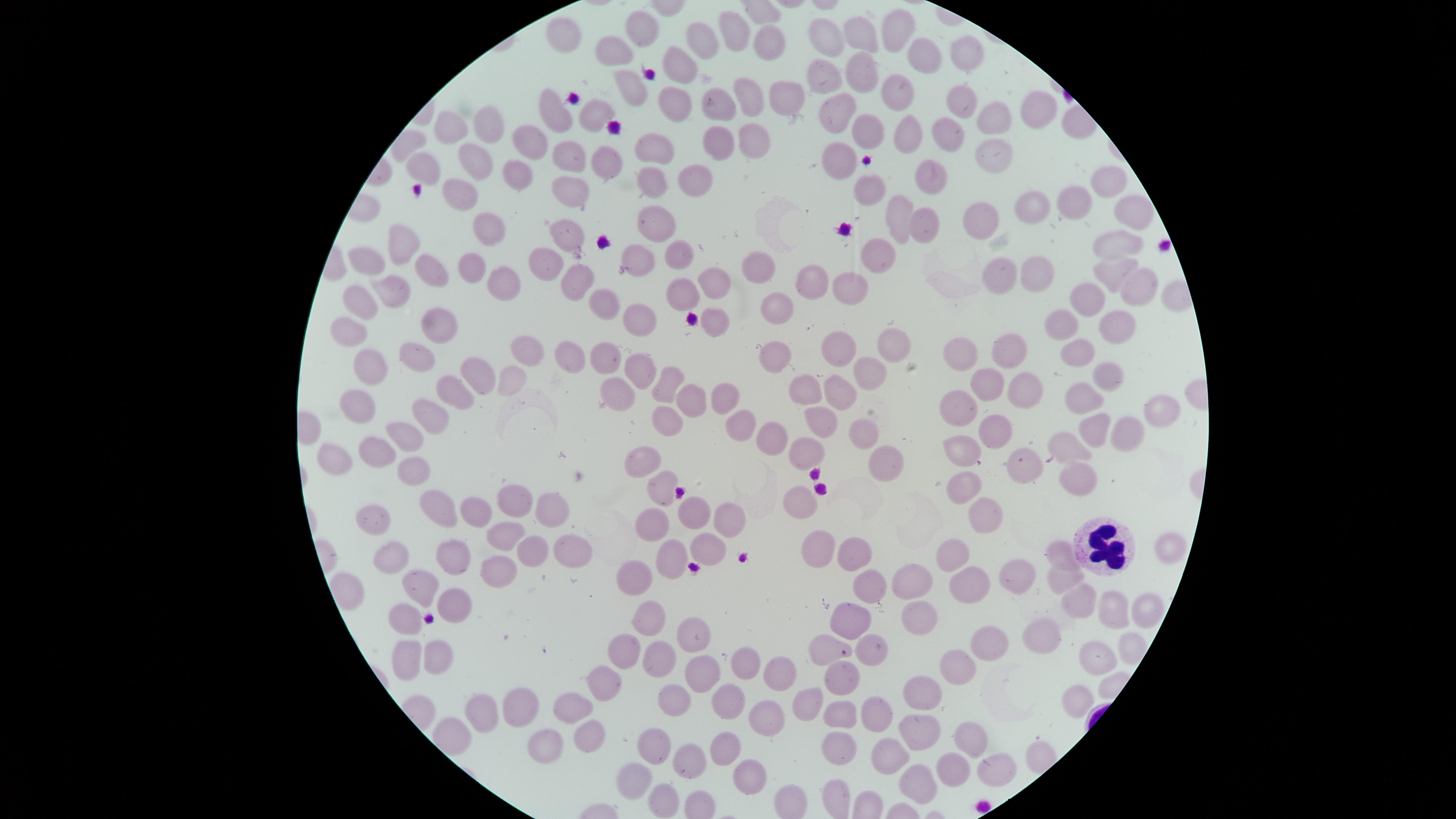 Approximate marker points as [x, y] in pixels. White blood cells: [1100, 549]. Uninfected red blood cells: [897, 26], [644, 29], [734, 29], [857, 30], [565, 37], [829, 37], [766, 39], [698, 43], [923, 52], [610, 53], [966, 54], [678, 66], [860, 70], [822, 78], [627, 87], [890, 88], [777, 93], [748, 94], [956, 95], [669, 98], [554, 104], [712, 104], [591, 111], [1032, 111], [843, 112], [991, 118], [491, 121], [452, 123], [940, 132], [867, 134], [902, 136], [751, 138], [714, 141], [533, 143], [648, 145], [572, 152], [985, 154], [601, 156], [472, 157], [832, 157], [428, 167], [655, 175], [692, 175], [929, 175], [522, 177], [1109, 179], [870, 189], [568, 190], [458, 194], [1033, 208], [1069, 209], [896, 213], [1133, 213], [658, 219], [980, 220], [920, 224], [484, 226], [567, 234], [401, 237], [1118, 242], [640, 251], [366, 255], [679, 255], [871, 259], [549, 262], [760, 264], [435, 266], [470, 271], [1105, 272], [1041, 273], [811, 276], [1003, 276], [385, 284], [709, 285], [510, 286], [568, 286], [848, 287], [1133, 288], [677, 293], [360, 297], [599, 297], [779, 302], [1091, 302], [637, 314], [714, 318], [1120, 321], [428, 325], [1066, 326], [349, 331], [881, 342], [837, 346], [1013, 348], [525, 351], [413, 352], [605, 352], [961, 352], [1070, 354], [560, 355], [783, 355], [365, 366], [635, 367], [864, 370], [481, 372], [1106, 372], [510, 376], [669, 381], [979, 383], [1016, 387], [448, 389], [800, 391], [725, 393], [611, 394], [833, 394], [692, 396], [1083, 398], [357, 405], [953, 406], [1162, 411], [432, 414], [663, 416], [816, 420], [866, 423], [742, 425], [1098, 425], [990, 428], [1126, 432], [398, 434], [775, 436], [1071, 443], [964, 446], [813, 450], [375, 451], [329, 454], [640, 456], [882, 458], [1022, 463], [412, 469], [1072, 476], [661, 480], [965, 486], [516, 496], [799, 500], [439, 506], [475, 511], [693, 511], [374, 514], [990, 514], [549, 518], [729, 520], [643, 524], [499, 534], [823, 543], [568, 547], [707, 547], [1058, 547], [865, 548], [1166, 549], [453, 550], [381, 552], [527, 552], [670, 552], [955, 552], [493, 573], [636, 575], [1007, 575], [1058, 580], [917, 582], [973, 582], [418, 583], [873, 589], [1073, 599], [456, 604], [1109, 610], [1143, 613], [649, 616], [402, 620], [919, 620], [850, 622], [1046, 629], [694, 632], [980, 638], [820, 646], [1134, 646], [434, 650], [622, 650], [656, 651], [864, 654], [1099, 656], [400, 658], [746, 659], [959, 669], [845, 675], [700, 677], [605, 678], [777, 679], [923, 690], [1069, 693], [519, 695], [671, 696], [726, 696], [805, 697], [571, 702], [480, 703], [877, 712], [766, 714], [841, 714], [915, 727], [589, 732], [542, 734], [652, 739], [972, 741], [720, 750], [837, 752], [893, 753], [686, 759], [990, 764], [634, 770], [747, 770], [951, 770], [910, 780], [661, 797]. Giemsa stain. Photographed with a smartphone camera through the microscope eyepiece. Thin blood smear. Circular visible region. Image is 1456×819 pixels. Single field of view. Presence: no malaria parasites identified.